Evaluate for Plasmodium parasites.
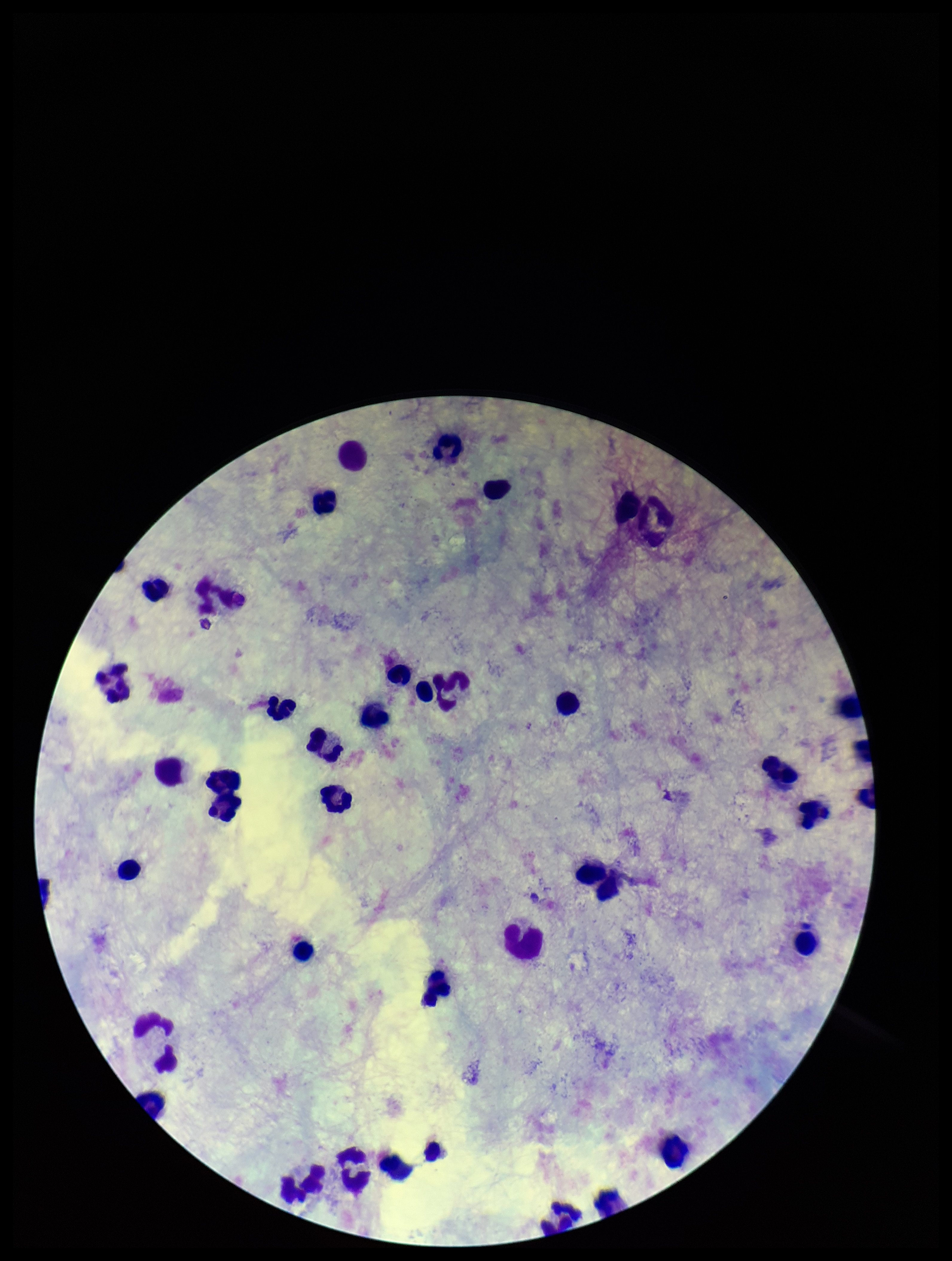
None detected.

Summary:
  - Field of view: one from this slide
  - Stain: Giemsa
  - Image size: 952×1261 pixels
  - Preparation: thick blood smear
  - Leukocyte count: 41
  - Capture: smartphone photograph through the microscope eyepiece
  - Patient malaria status: negative
  - Parasite count: 0